Name the parasite shown.
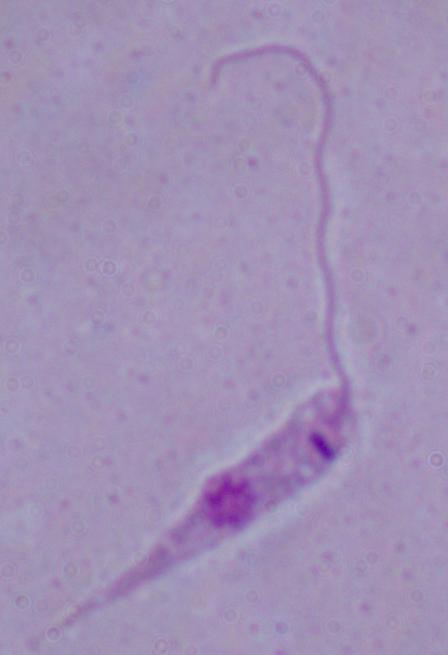

This is Leishmania.

Summary:
  - Modality: photomicrograph
  - Magnification: 1000x